Name the parasite shown.
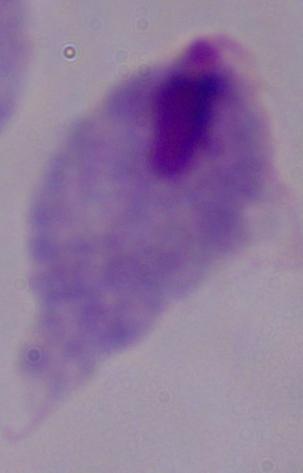

This is a trichomonad.

{
  "modality": "photomicrograph",
  "magnification": "1000x"
}